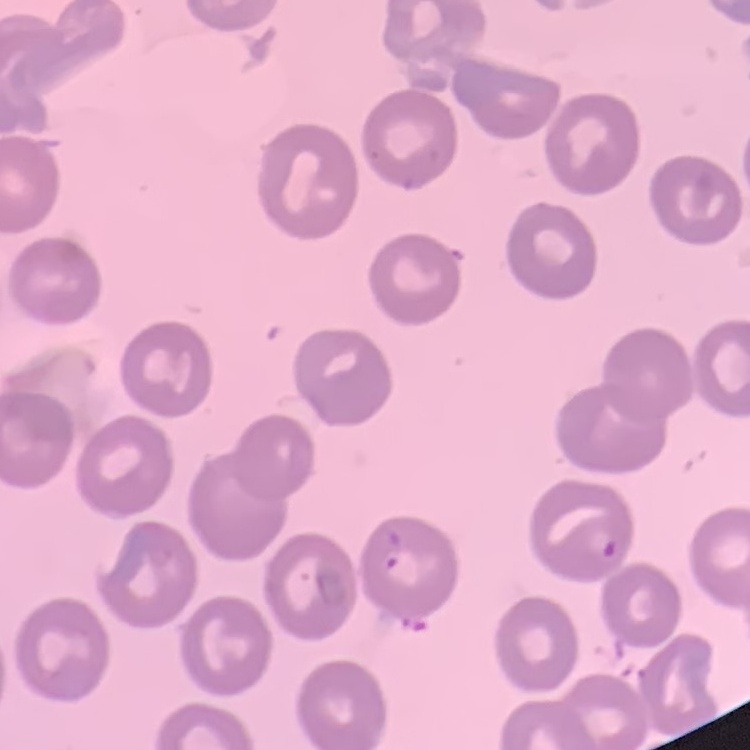
The erythrocytes show no rouleaux formation. Thin blood smear. Field's or Giemsa stain. Square crop of a larger photomicrograph.